Locate malaria parasites and leukocytes.
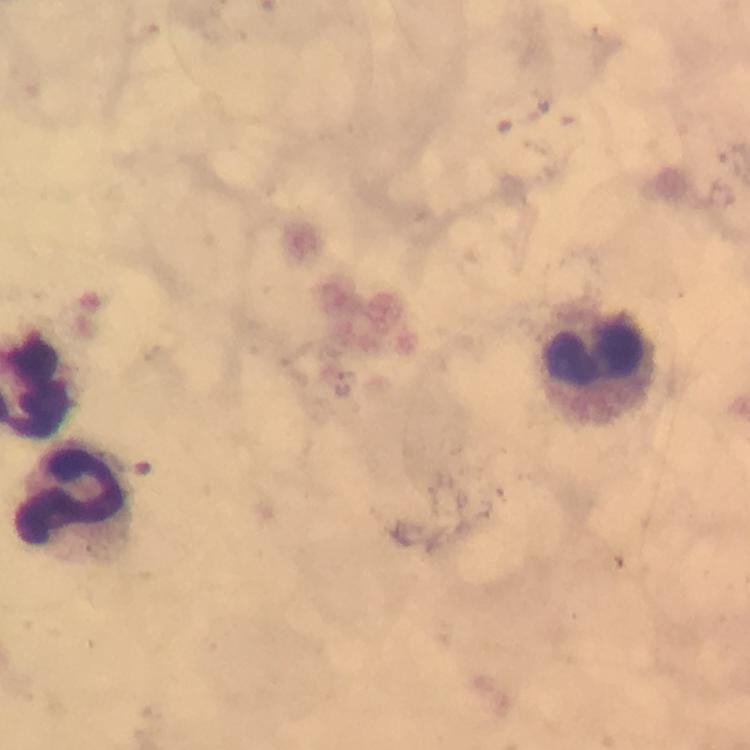

Approximate centers as {x, y} in pixels.
Malaria parasites: {342, 384}.
Leukocytes: {597, 361}, {81, 501}.

Giemsa-stained preparation. Immersion oil was used. Smartphone photograph taken through a microscope. 100x magnification. A crop from one field of view. From a diagnostic examination for malaria. Thick blood film. Image is 750×750 pixels.